Identify the blood parasite species.
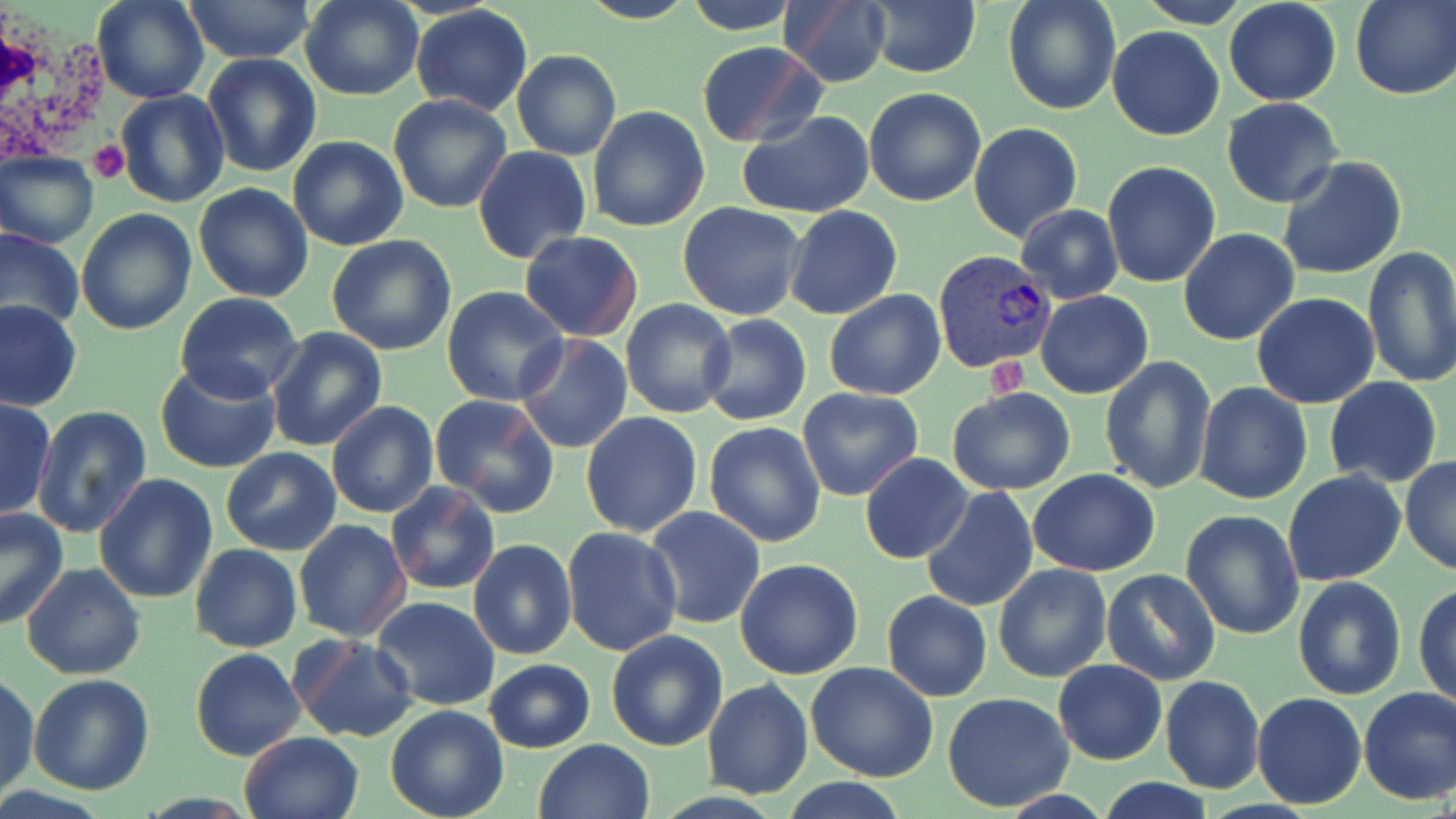

Plasmodium vivax.

white_blood_cell_locations: 'approximate bounding boxes as (x1,y1)-(x2,y2) corner pairs in pixels: (0,11)-(116,175)'
platelet_locations: 'approximate bounding boxes as (x1,y1)-(x2,y2) corner pairs in pixels: (87,141)-(127,183), (986,353)-(1027,394)'
stain: May-Grünwald-Giemsa
plasmodium_vivax_infected_red_blood_cell_locations: 'approximate bounding boxes as (x1,y1)-(x2,y2) corner pairs in pixels: (932,251)-(1056,373)'
image_size: 1456×819 pixels
magnification: 1000x
uninfected_red_blood_cell_locations: 'approximate bounding boxes as (x1,y1)-(x2,y2) corner pairs in pixels: (92,0)-(209,105), (300,0)-(422,101), (577,0)-(698,25), (682,0)-(802,34), (1002,0)-(1122,116), (1136,0)-(1251,27), (1224,0)-(1342,106), (1350,0)-(1455,99), (184,1)-(315,66), (776,2)-(893,88), (865,2)-(981,78), (411,5)-(533,117), (1107,25)-(1225,141), (695,40)-(826,148), (512,50)-(621,161), (202,53)-(322,177), (862,87)-(986,208), (116,89)-(230,208), (387,94)-(511,213), (1222,98)-(1345,208), (587,106)-(710,230), (737,110)-(875,219), (969,121)-(1082,241), (287,136)-(408,250), (473,146)-(591,264), (1,150)-(99,248), (1275,156)-(1407,280), (1100,161)-(1221,287), (192,183)-(314,303), (677,201)-(806,321), (1016,203)-(1123,305), (785,205)-(903,320), (75,209)-(195,335), (0,226)-(85,332), (1179,228)-(1300,346), (518,231)-(644,341), (326,233)-(456,356), (1362,246)-(1456,389), (441,287)-(569,407), (824,289)-(945,400), (1035,291)-(1153,399), (176,293)-(303,403), (1252,293)-(1380,408), (0,298)-(83,412), (621,300)-(738,419), (700,314)-(812,426), (265,327)-(388,452), (515,334)-(634,456), (1100,356)-(1217,493), (154,362)-(282,475), (1324,377)-(1441,489), (1193,383)-(1312,504), (797,386)-(924,502), (947,387)-(1076,494), (429,396)-(560,518), (0,397)-(55,521), (326,400)-(439,519), (31,405)-(154,540), (580,411)-(704,538), (703,422)-(828,547), (222,448)-(342,556), (860,454)-(971,562), (1400,457)-(1456,575), (1029,468)-(1160,576), (1282,472)-(1407,587), (94,475)-(218,605), (387,483)-(499,597), (918,485)-(1037,612), (417,498)-(552,635), (644,506)-(766,630), (0,509)-(69,629), (1180,510)-(1304,641), (294,520)-(413,642), (561,526)-(683,657), (468,539)-(577,660), (190,543)-(301,652), (734,559)-(863,680), (21,564)-(145,680), (991,564)-(1111,683), (1100,567)-(1220,686), (1293,576)-(1407,701), (1414,582)-(1456,708), (882,590)-(993,702), (371,597)-(501,711), (606,630)-(727,751), (290,633)-(418,743), (191,648)-(306,762), (485,659)-(596,752), (1053,659)-(1167,765), (806,662)-(939,782), (1,672)-(40,799), (28,672)-(157,794), (1159,675)-(1265,792), (702,680)-(814,800), (1356,686)-(1456,803), (942,692)-(1075,810), (1250,693)-(1365,810), (385,704)-(509,819), (238,731)-(365,819), (532,739)-(655,819), (782,779)-(909,819), (1093,779)-(1219,818)'
preparation: thin blood smear
modality: light microscopy
field_of_view: single